Assess this cell for malaria.
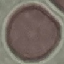
Uninfected.

Summary:
  - Capture: smartphone camera at the microscope eyepiece
  - Stain: Giemsa
  - Preparation: thin smear
  - Image type: automatically extracted cell patch, resized to 64 × 64 pixels